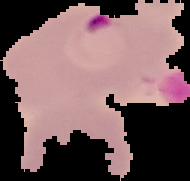

preparation = thin blood film
malaria status = parasitized
image size = 190×181 pixels
image type = segmented cell region with the area outside set to black